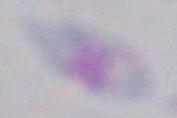
magnification = 1000x
identification = Toxoplasma gondii
modality = micrograph